State which parasite is depicted.
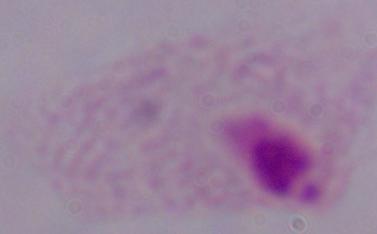
A trichomonad.

1000x magnification. Photomicrograph.